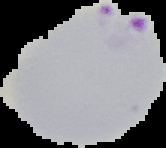 Malaria status: parasitized. From a thin blood smear. Cell region segmented out of the field of view; the surrounding area is masked to black. Image is 166×148 pixels.